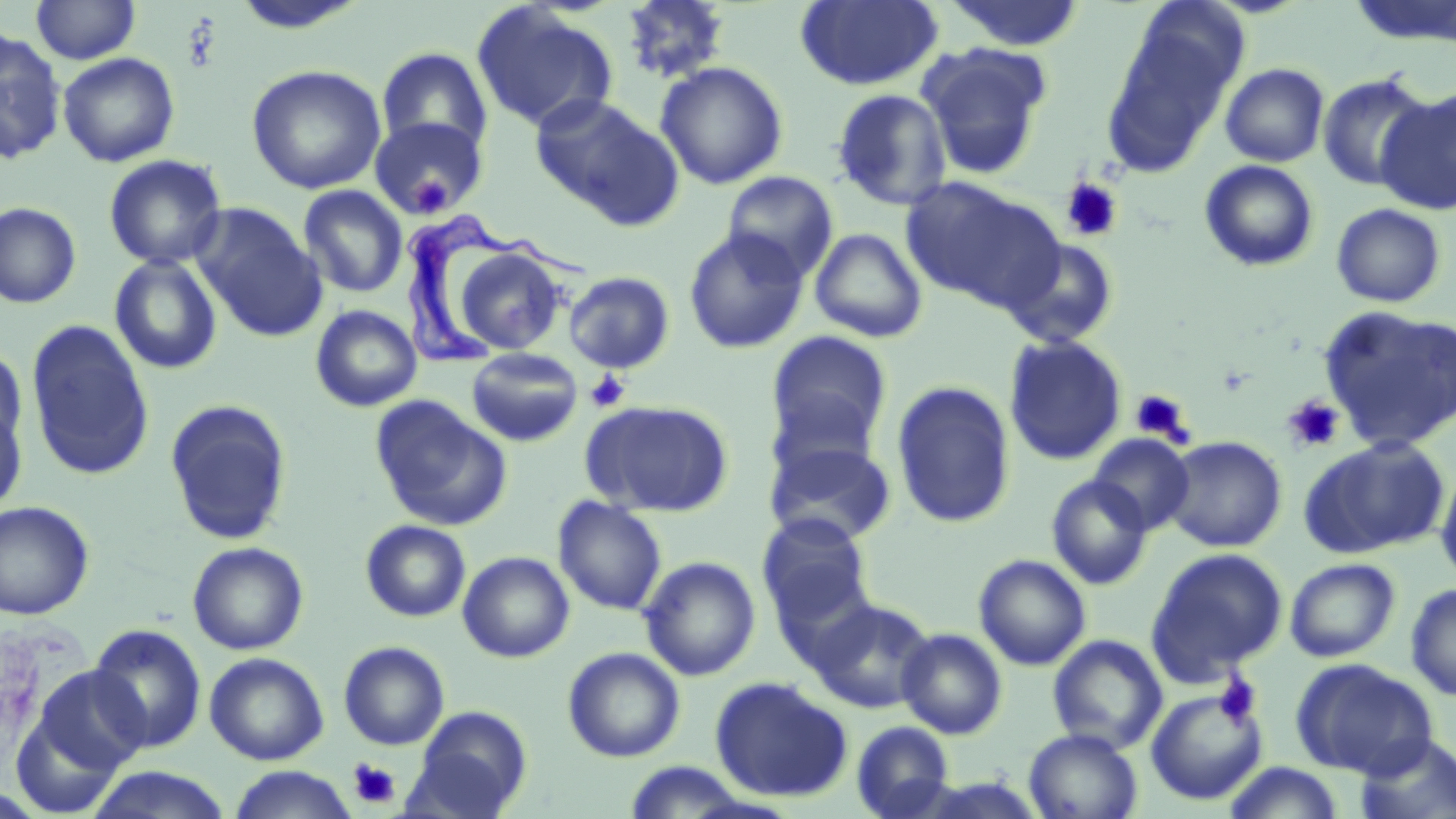
{
  "slide_level_diagnosis": "Trypanosoma brucei",
  "modality": "light microscopy",
  "platelet_locations": "approximate bounding boxes as (x1, y1, x2, y2) in pixels: (410, 178, 455, 215), (1059, 178, 1124, 243), (585, 370, 632, 412), (1129, 389, 1194, 445), (1283, 395, 1345, 453), (1215, 674, 1263, 728), (348, 758, 400, 810)",
  "trypanosoma_brucei_locations": "approximate bounding boxes as (x1, y1, x2, y2) in pixels: (404, 214, 599, 372)",
  "field_of_view": "single",
  "magnification": "1000x",
  "stain": "May-Grünwald-Giemsa",
  "image_size": "1456×819 pixels",
  "uninfected_red_blood_cell_locations": "approximate bounding boxes as (x1, y1, x2, y2) in pixels: (31, 0, 141, 64), (619, 0, 732, 84), (795, 0, 944, 91), (941, 0, 1087, 52), (471, 3, 619, 134), (1100, 16, 1242, 176), (0, 28, 68, 165), (916, 42, 1052, 181), (376, 47, 493, 160), (57, 51, 180, 167), (655, 61, 789, 190), (1220, 63, 1330, 167), (246, 64, 386, 194), (1318, 72, 1434, 191), (831, 89, 952, 211), (1376, 89, 1456, 215), (530, 92, 684, 227), (370, 116, 488, 221), (103, 154, 228, 270), (1199, 160, 1319, 272), (722, 170, 838, 281), (902, 177, 1061, 311), (298, 185, 408, 299), (0, 202, 82, 309), (191, 203, 326, 341), (1330, 203, 1448, 308), (683, 228, 809, 354), (808, 228, 929, 343), (1001, 237, 1120, 350), (454, 246, 566, 355), (109, 255, 223, 375), (563, 270, 676, 374), (1318, 304, 1456, 453), (310, 305, 423, 413), (25, 319, 155, 481), (766, 330, 893, 459), (1003, 335, 1127, 466), (0, 345, 28, 455), (466, 347, 583, 447), (890, 380, 1016, 529), (370, 395, 510, 531), (0, 398, 28, 515), (164, 399, 292, 546), (581, 399, 735, 517), (1088, 434, 1195, 535), (1162, 435, 1287, 552), (1298, 436, 1452, 559), (763, 438, 897, 547), (1436, 460, 1456, 587), (1046, 474, 1154, 590), (552, 496, 668, 616), (0, 500, 95, 620), (757, 514, 875, 624), (360, 520, 471, 622), (187, 541, 309, 655), (1145, 547, 1288, 685), (457, 551, 574, 663), (973, 553, 1091, 671), (639, 556, 761, 681), (1284, 558, 1401, 662), (1405, 583, 1456, 702), (807, 597, 937, 714), (87, 624, 207, 752), (896, 627, 1008, 739), (1047, 634, 1168, 754), (339, 640, 450, 750), (562, 646, 686, 763), (204, 652, 329, 764), (1290, 658, 1437, 778), (23, 663, 151, 786), (710, 677, 852, 802), (1145, 687, 1268, 805), (406, 706, 533, 819), (851, 720, 954, 818), (1024, 728, 1143, 818), (1353, 733, 1456, 819), (1221, 761, 1347, 819), (227, 766, 358, 818), (80, 767, 236, 819)",
  "preparation": "thin blood film"
}